Identify the cell.
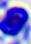
This is a leukocyte.

modality: photomicrograph
magnification: 400x